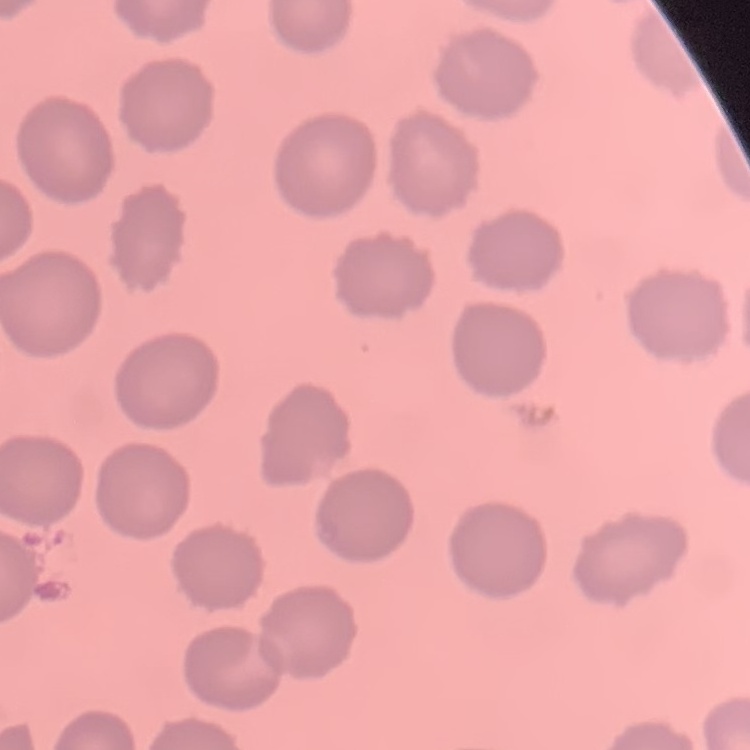

The red blood cells exhibit no rouleaux formation. Field's or Giemsa stain. Thin blood film. One tile cut from a larger photomicrograph.